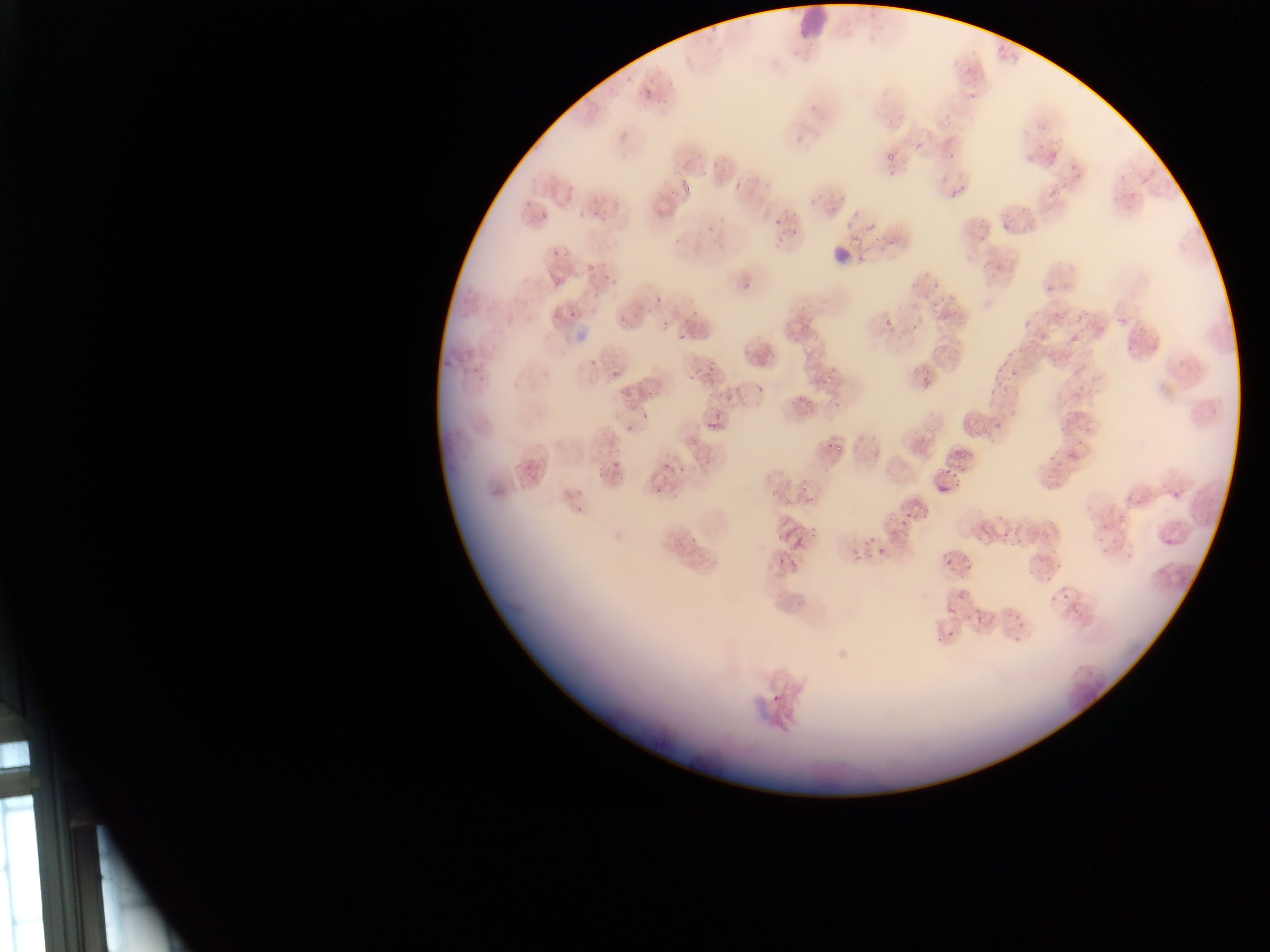

malaria_parasite_locations: 'approximate bounding boxes as left top right bottom in pixels: 960 60 973 78; 618 76 638 87; 641 89 652 100; 964 93 977 101; 657 96 669 106; 943 112 956 126; 620 128 638 140; 814 129 822 141; 914 141 922 149; 695 151 706 160; 711 152 723 167; 887 152 898 164; 1047 152 1057 166; 945 153 958 161; 1069 161 1076 170; 1071 172 1082 180; 680 179 690 191; 564 182 578 198; 951 182 963 198; 731 184 742 192; 666 186 677 198; 1046 190 1060 201; 590 200 612 218; 830 202 840 214; 654 203 667 217; 540 210 546 219; 851 211 859 220; 772 218 781 227; 705 221 721 236; 999 221 1008 232; 1019 222 1030 234; 866 224 873 232; 791 228 799 237; 672 235 680 245; 887 235 898 248; 975 235 986 243; 873 237 876 245; 858 238 872 255; 553 248 561 256; 586 262 597 269; 546 271 554 279; 603 271 613 278; 552 278 565 287; 739 285 750 296; 1044 285 1053 292; 654 294 664 304; 931 294 947 314; 946 295 954 303; 687 300 704 322; 615 306 632 323; 568 307 580 319; 641 308 651 316; 1055 312 1068 320; 1078 313 1090 324; 1116 315 1129 323; 884 317 893 327; 806 318 817 324; 911 321 921 333; 661 322 668 330; 1128 325 1142 335; 1038 331 1050 343; 678 334 687 342; 1069 334 1080 343; 1007 347 1025 356; 743 357 751 363; 589 358 598 368; 706 361 716 371; 911 362 922 373; 471 365 483 371; 803 367 813 376; 692 368 703 376; 610 370 620 380; 995 371 1004 378; 826 373 832 383; 921 373 931 385; 618 382 633 398; 756 383 769 394; 645 387 657 398; 826 390 832 399; 987 391 995 396; 711 394 716 402; 723 395 734 409; 802 403 812 407; 1066 409 1081 427; 642 413 653 422; 703 416 724 431; 994 420 1004 430; 983 421 992 427; 624 423 634 436; 1077 432 1091 446; 823 437 837 451; 1048 455 1056 464; 945 457 965 486; 616 458 624 471; 526 461 534 470; 662 462 673 473; 595 463 607 477; 678 466 687 475; 936 484 947 493; 653 485 663 494; 1170 487 1186 500; 780 498 788 505; 805 500 814 506; 920 507 930 520; 900 514 910 524; 1040 527 1053 539; 785 529 796 538; 865 535 876 545; 791 536 803 551; 996 538 1013 551; 878 545 888 553; 1049 550 1058 557; 864 551 873 560; 776 552 786 563; 790 555 802 564; 944 555 953 565; 960 556 970 570; 1033 562 1043 570; 956 570 968 578; 1050 591 1056 605; 956 593 964 600; 1014 609 1024 622; 1011 628 1022 642; 771 692 783 705 | approximate x y pixel centers of objects too small to bound: 1128 348; 1015 372; 803 488; 1059 566; 1050 579; 1065 597; 949 612; 950 636'
country: Ghana
leukocyte_locations: 'approximate bounding boxes as left top right bottom in pixels: 792 5 833 37; 830 236 857 263'
capture: mobile-phone photograph through a microscope
image_size: 1270×952 pixels
preparation: thin blood film
field_of_view: single